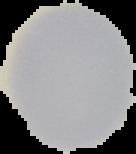

result: no Plasmodium parasites detected
preparation: thin blood film
image_type: segmented cell region with the area outside set to black
image_size: 136×154 pixels